Report the malaria status of this cell.
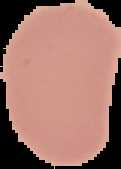
It is uninfected.

image type = segmented cell region with the area outside set to black
preparation = thin blood smear
image size = 121×169 pixels